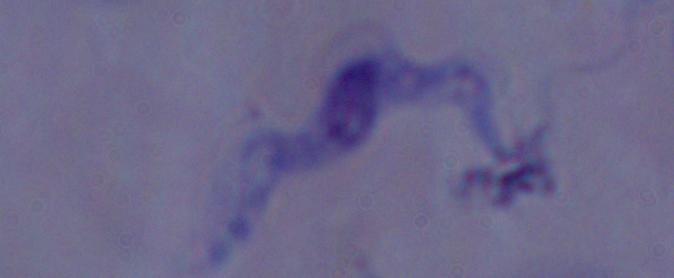
A trypanosome is shown. Micrograph. 1000x magnification.